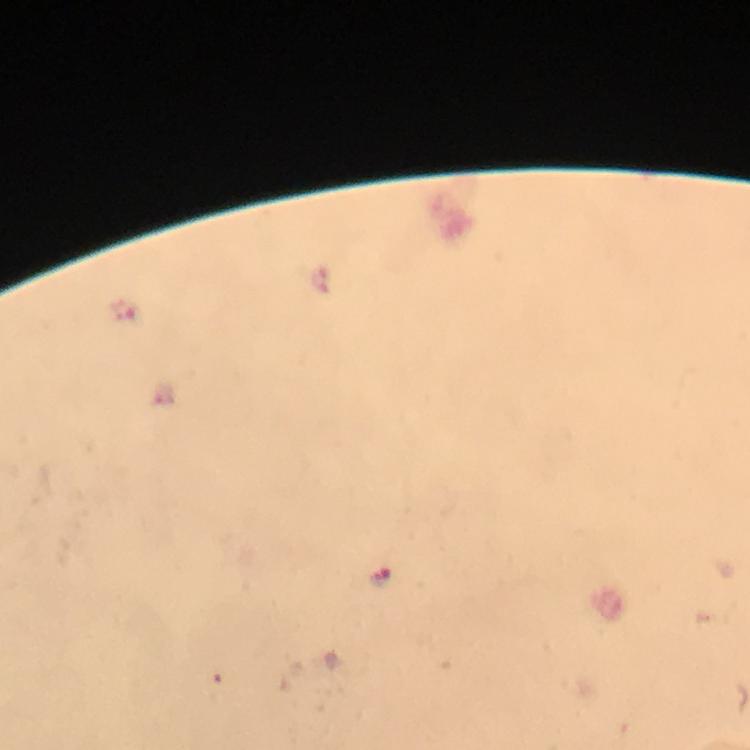

Approximate centers as {x, y} in pixels.
Summary:
  - Malaria parasite locations: {126, 310}, {380, 577}
  - Context: from a diagnostic examination for malaria
  - Capture: smartphone mounted on the microscope
  - Magnification: 100x
  - Cropped from: a single field of view
  - Stain: Giemsa
  - Immersion oil: used
  - Preparation: thick blood film
  - Image size: 750×750 pixels